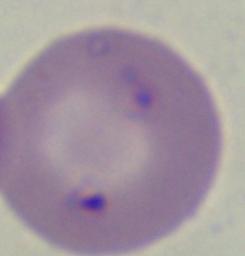

Captured at 1000x magnification. Micrograph. A Babesia parasite is seen.